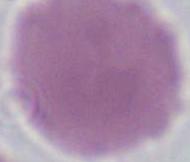

Summary:
  - Identification: red blood cell
  - Modality: micrograph
  - Magnification: 1000x